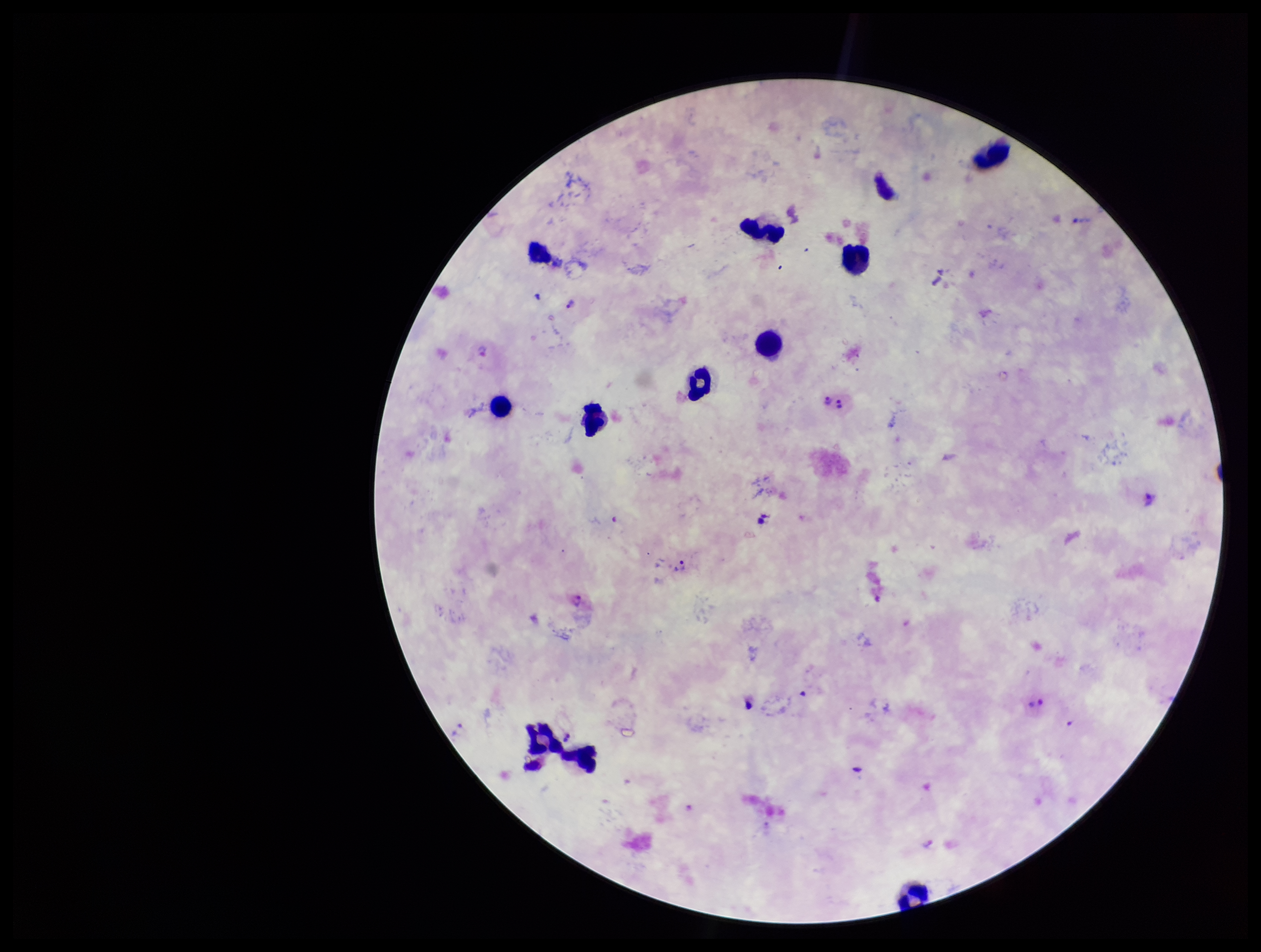

Parasite count: 5. Plasmodium parasites: identified. Leukocyte count: 10. Photographed through the microscope eyepiece with a smartphone camera. Preparation: thick. Giemsa stain. Image is 1261×952 pixels. Species reported for this patient: Plasmodium vivax. Single field of view. Patient malaria status: positive.